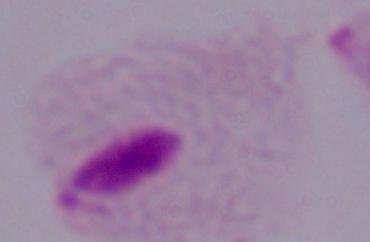

Summary:
  - Modality: micrograph
  - Identification: trichomonad
  - Magnification: 1000x